Name the parasite shown.
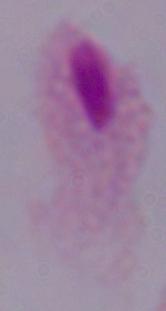

This is a trichomonad.

magnification = 1000x
modality = photomicrograph